Assess this cell for malaria.
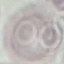

It is uninfected.

Summary:
  - Preparation: thin blood smear
  - Stain: Giemsa
  - Capture: smartphone camera at the microscope eyepiece
  - Image type: automatically extracted cell patch, resized to 64 × 64 pixels